Outline each blood parasite and name the species.
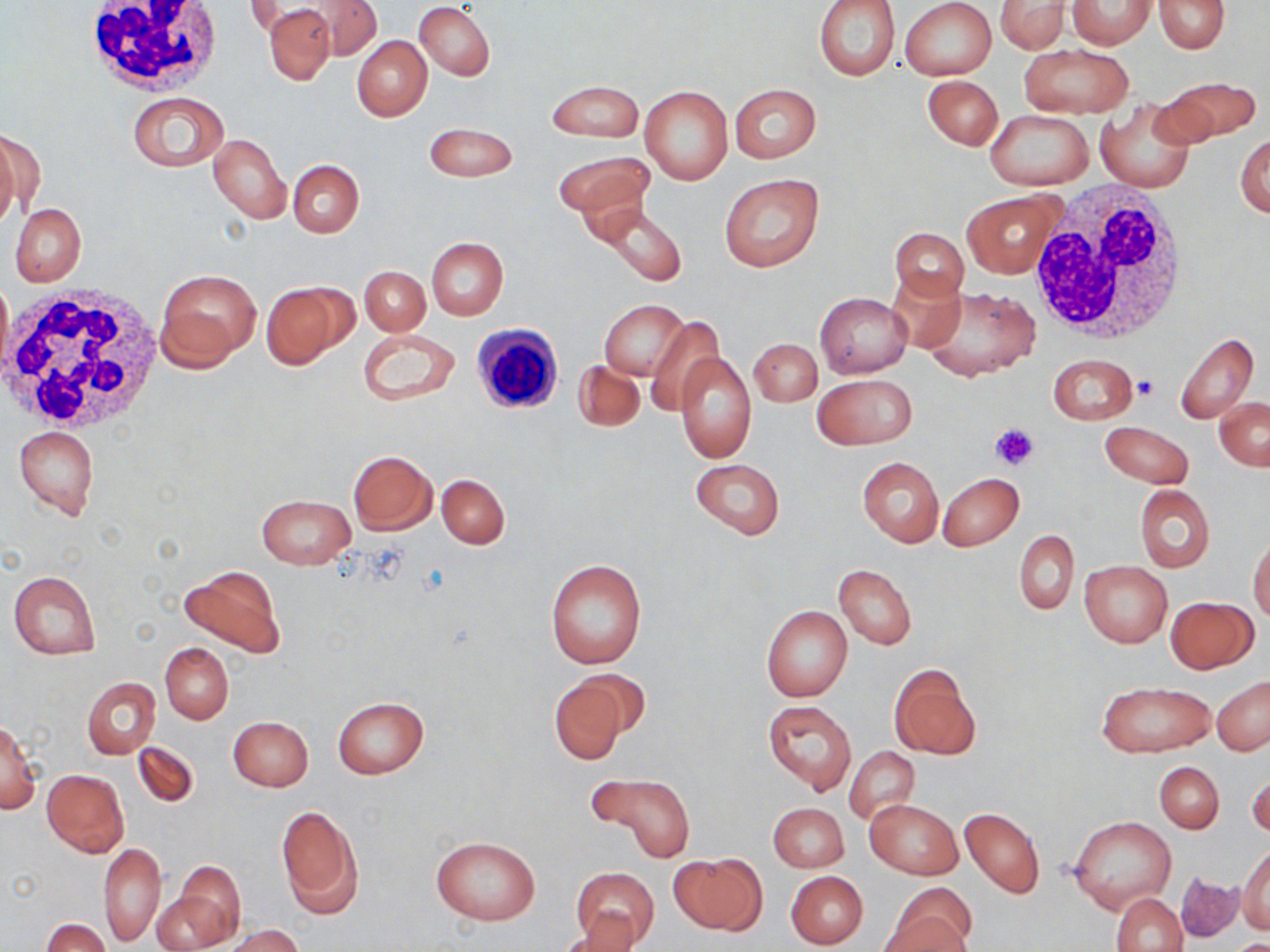
No blood parasites seen.

Summary:
  - Coordinate format: approximate bounding boxes as [x1, y1, x2, y2] in pixels
  - Uninfected red blood cell locations: [814, 0, 900, 80], [901, 0, 996, 81], [1155, 0, 1229, 52], [303, 1, 382, 60], [995, 1, 1072, 53], [1068, 1, 1156, 49], [258, 2, 339, 82], [415, 3, 495, 80], [353, 36, 432, 121], [1018, 44, 1135, 119], [923, 75, 1003, 150], [1156, 77, 1262, 145], [545, 80, 644, 142], [729, 83, 821, 163], [640, 85, 732, 185], [127, 92, 228, 171], [1097, 100, 1197, 194], [983, 110, 1095, 190], [423, 124, 518, 182], [0, 129, 35, 227], [1236, 132, 1270, 218], [209, 133, 290, 224], [554, 151, 655, 221], [288, 159, 364, 238], [718, 172, 824, 271], [962, 189, 1064, 279], [598, 203, 687, 288], [11, 204, 86, 286], [888, 227, 968, 306], [426, 237, 509, 320], [360, 265, 429, 335], [887, 269, 967, 351], [158, 270, 260, 366], [0, 274, 12, 376], [260, 281, 354, 369], [917, 286, 1040, 381], [816, 293, 912, 378], [601, 299, 688, 380], [645, 314, 723, 414], [358, 327, 460, 407], [1174, 333, 1260, 424], [748, 338, 822, 406], [674, 351, 756, 464], [1047, 354, 1137, 425], [573, 359, 644, 432], [813, 373, 917, 449], [1214, 397, 1269, 470], [1100, 422, 1193, 488], [14, 425, 99, 520], [348, 450, 437, 535], [690, 457, 785, 540], [857, 457, 944, 547], [938, 472, 1024, 551], [437, 475, 509, 548], [1134, 484, 1215, 572], [257, 494, 355, 569], [1015, 529, 1079, 614], [1248, 536, 1270, 623], [545, 557, 648, 670], [1079, 561, 1172, 646], [834, 564, 916, 648], [178, 566, 285, 657], [8, 570, 101, 660], [1166, 596, 1258, 673], [761, 605, 852, 701], [161, 642, 233, 724], [889, 664, 979, 760], [546, 671, 638, 765], [1212, 676, 1270, 756], [83, 677, 160, 759], [1096, 680, 1215, 756], [333, 696, 429, 779], [764, 700, 856, 794], [228, 716, 314, 791], [0, 721, 41, 815], [132, 741, 199, 807], [845, 745, 921, 824], [1155, 762, 1223, 833], [41, 769, 127, 858], [1248, 770, 1269, 843], [594, 774, 695, 863], [866, 799, 962, 880], [768, 802, 849, 872], [275, 804, 364, 920], [960, 807, 1045, 898], [1069, 815, 1175, 915], [430, 835, 540, 925], [99, 843, 165, 945], [1236, 846, 1270, 934], [673, 853, 764, 936], [170, 864, 246, 946], [570, 867, 660, 948], [785, 871, 868, 948], [1176, 871, 1242, 943], [889, 883, 977, 952], [153, 892, 229, 949], [1112, 892, 1187, 952], [41, 918, 109, 952], [561, 920, 646, 951], [223, 924, 303, 952]
  - Platelet locations: [1134, 375, 1159, 401], [990, 423, 1038, 471]
  - White blood cell locations: [79, 0, 226, 96], [1024, 183, 1195, 348], [1, 286, 165, 437], [472, 323, 565, 415]
  - Slide-level diagnosis: no evidence of blood parasites
  - Stain: May-Grünwald-Giemsa
  - Image size: 1270×952 pixels
  - Magnification: 1000x
  - Preparation: thin blood film
  - Field of view: single
  - Modality: optical microscopy